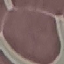

malaria_status: uninfected
capture: smartphone camera at the microscope eyepiece
image_type: cell patch, automatically extracted from a larger field of view and resized to 64 × 64 pixels
preparation: thin blood smear
stain: Giemsa